Identify the blood parasite species.
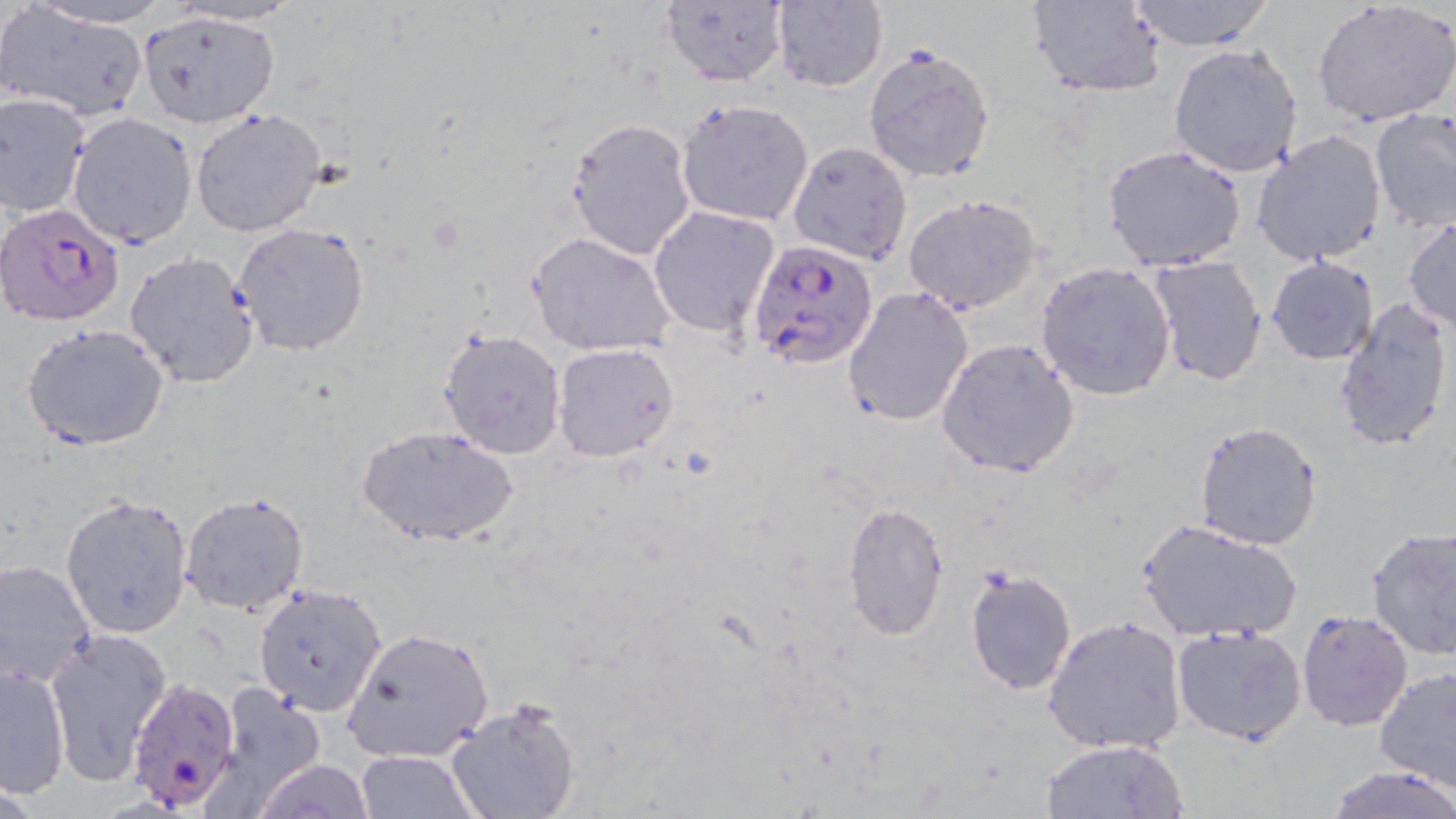

Plasmodium falciparum.

Approximate bounding boxes as [x1, y1, x2, y2] in pixels. Plasmodium falciparum-infected red blood cell locations: [0, 200, 126, 330], [748, 238, 878, 369], [125, 676, 243, 814]. Uninfected red blood cell locations: [22, 0, 174, 28], [658, 0, 788, 87], [770, 0, 889, 93], [1025, 0, 1167, 97], [1124, 0, 1276, 50], [1312, 2, 1456, 128], [0, 4, 151, 123], [135, 9, 280, 128], [1169, 44, 1302, 178], [864, 47, 997, 181], [1, 91, 93, 217], [675, 98, 815, 227], [190, 107, 327, 237], [1369, 108, 1456, 231], [67, 113, 200, 249], [564, 118, 698, 261], [1252, 130, 1387, 268], [785, 141, 913, 266], [1101, 145, 1247, 273], [902, 193, 1042, 316], [648, 205, 780, 341], [1403, 219, 1456, 332], [232, 222, 370, 356], [526, 233, 678, 358], [123, 252, 260, 387], [1265, 255, 1379, 365], [1146, 256, 1268, 388], [1034, 260, 1176, 400], [842, 286, 975, 429], [1331, 298, 1453, 452], [23, 322, 169, 451], [436, 327, 567, 461], [935, 337, 1081, 479], [551, 343, 680, 463], [1193, 420, 1323, 549], [356, 426, 519, 548], [60, 492, 195, 640], [180, 492, 309, 614], [840, 503, 950, 641], [1135, 519, 1302, 643], [1366, 525, 1456, 664], [0, 559, 98, 688], [963, 565, 1078, 697], [251, 583, 388, 718], [1295, 610, 1414, 733], [1043, 615, 1187, 755], [1172, 625, 1306, 746], [343, 628, 495, 763], [43, 631, 170, 787], [1, 665, 70, 796], [1371, 666, 1456, 795], [214, 687, 331, 807], [446, 699, 579, 819], [1039, 738, 1190, 819], [356, 750, 479, 818], [255, 758, 374, 819], [1323, 762, 1455, 819]. Image is 1456×819 pixels. Light microscopy. One field of a larger specimen. May-Grünwald-Giemsa-stained preparation. Thin blood smear. 1000x magnification.